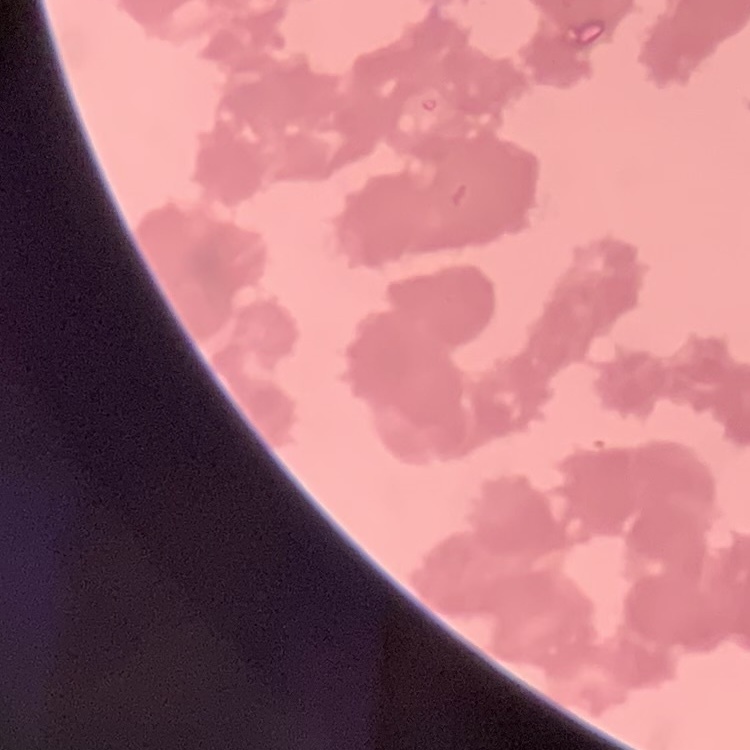
Summary:
  - Red blood cell morphology: rouleaux formation
  - Image type: square crop of a larger photomicrograph
  - Preparation: thin peripheral smear
  - Stain: Field's or Giemsa